Locate every Plasmodium parasite by life-cycle stage, and every leukocyte.
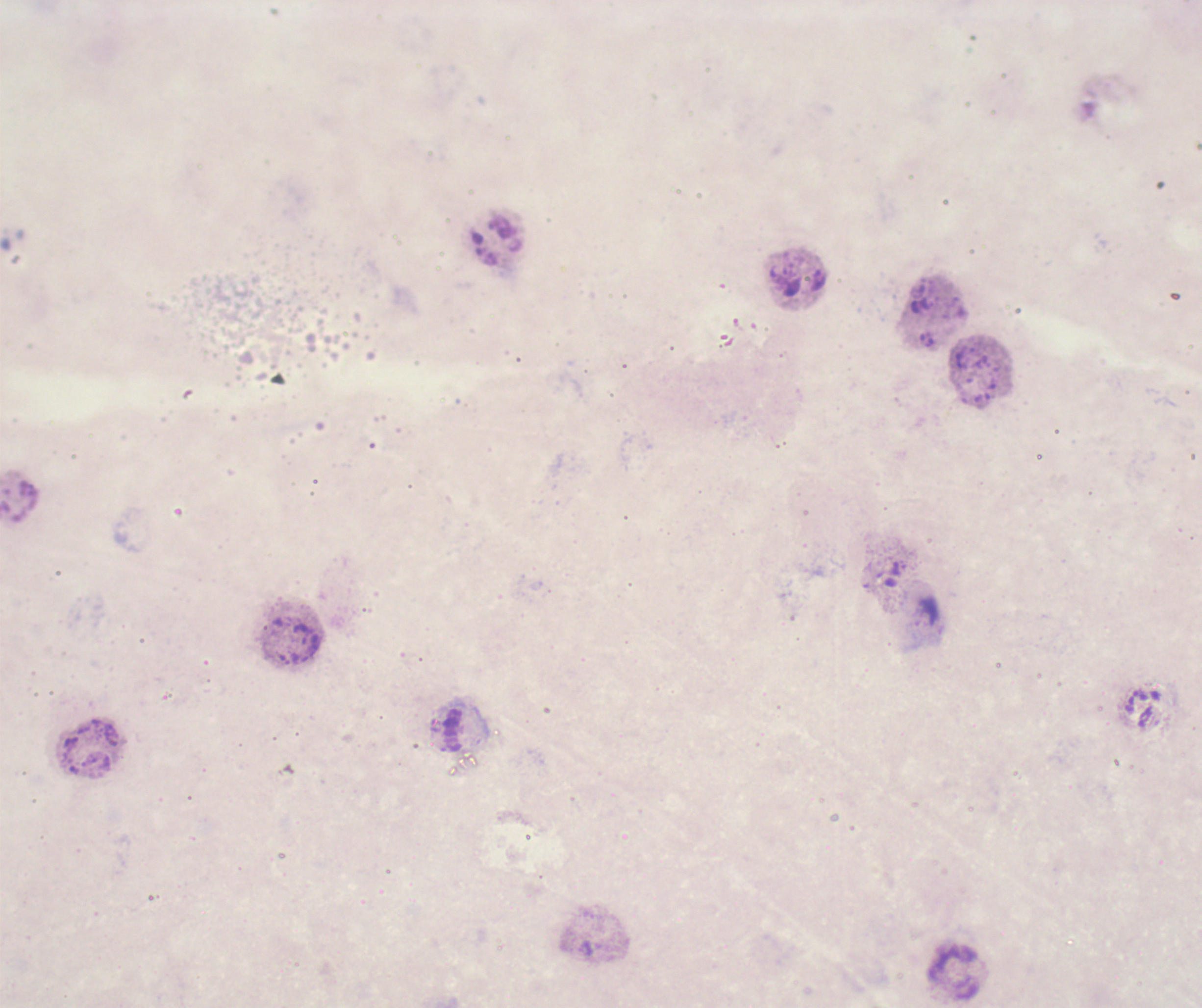
No Plasmodium parasites detected.
Approximate centers as (x, y) in pixels.
Leukocytes: (495, 242), (450, 728), (954, 974).

Background quality: poor. Romanowsky-stained preparation. Coloration quality: bad. Thick blood smear. Image is 1202×1008 pixels. One field from this slide. Captured at 100x magnification. Previously used in an actual diagnosis.